Name the cell type shown.
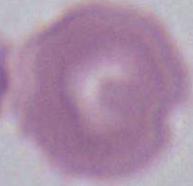
An erythrocyte.

Summary:
  - Magnification: 1000x
  - Modality: micrograph